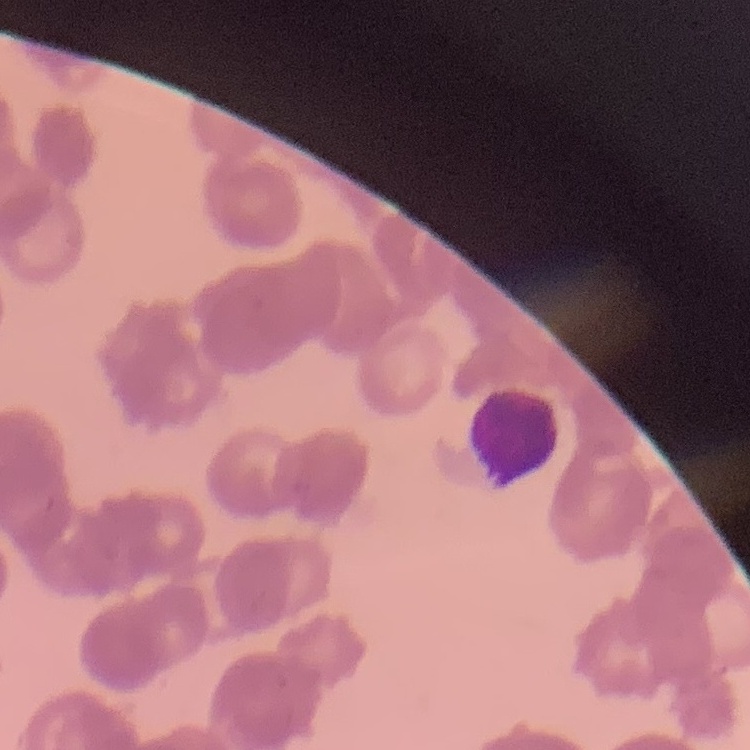 The erythrocytes exhibit rouleaux formation. Field's or Giemsa stain. Thin blood film. One tile cut from a larger photomicrograph.